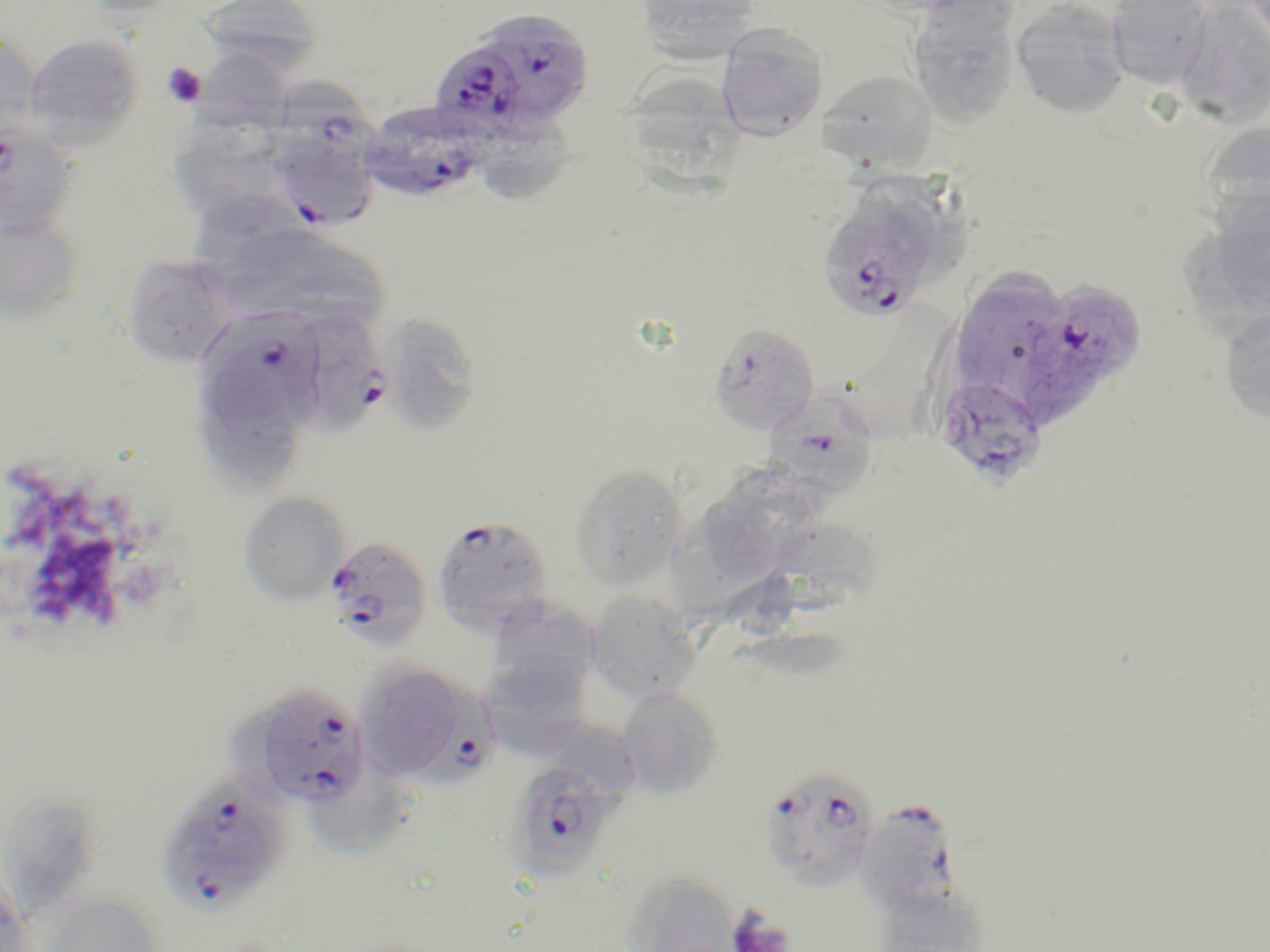

{
  "slide_level_diagnosis": "Plasmodium falciparum",
  "uninfected_red_blood_cell_locations": "approximate bounding boxes as named x1/y1/x2/y2 corners in pixels: (x1=72, y1=0, x2=190, y2=20), (x1=200, y1=0, x2=321, y2=78), (x1=634, y1=0, x2=763, y2=63), (x1=851, y1=0, x2=981, y2=15), (x1=1009, y1=1, x2=1131, y2=119), (x1=1106, y1=1, x2=1214, y2=91), (x1=1177, y1=1, x2=1270, y2=124), (x1=906, y1=4, x2=1022, y2=129), (x1=716, y1=24, x2=828, y2=141), (x1=0, y1=32, x2=43, y2=138), (x1=24, y1=34, x2=143, y2=150), (x1=194, y1=49, x2=292, y2=135), (x1=627, y1=69, x2=753, y2=204), (x1=817, y1=70, x2=937, y2=171), (x1=482, y1=106, x2=581, y2=204), (x1=176, y1=118, x2=279, y2=234), (x1=1202, y1=118, x2=1269, y2=238), (x1=199, y1=198, x2=313, y2=299), (x1=0, y1=213, x2=85, y2=326), (x1=278, y1=242, x2=390, y2=337), (x1=121, y1=254, x2=240, y2=368), (x1=954, y1=266, x2=1066, y2=381), (x1=1218, y1=306, x2=1270, y2=423), (x1=379, y1=312, x2=485, y2=438), (x1=199, y1=397, x2=302, y2=484), (x1=569, y1=463, x2=689, y2=592), (x1=729, y1=463, x2=842, y2=523), (x1=239, y1=491, x2=351, y2=606), (x1=705, y1=492, x2=789, y2=586), (x1=774, y1=517, x2=890, y2=596), (x1=668, y1=518, x2=766, y2=623), (x1=585, y1=590, x2=703, y2=705), (x1=484, y1=600, x2=599, y2=702), (x1=485, y1=656, x2=586, y2=757), (x1=352, y1=660, x2=463, y2=784), (x1=614, y1=687, x2=725, y2=799), (x1=544, y1=716, x2=637, y2=811), (x1=311, y1=757, x2=408, y2=855), (x1=12, y1=791, x2=105, y2=917), (x1=621, y1=871, x2=740, y2=952), (x1=0, y1=880, x2=33, y2=952), (x1=42, y1=892, x2=167, y2=951), (x1=871, y1=897, x2=987, y2=952)",
  "modality": "light microscopy",
  "field_of_view": "single",
  "plasmodium_falciparum_infected_red_blood_cell_locations": "approximate bounding boxes as named x1/y1/x2/y2 corners in pixels: (x1=483, y1=11, x2=597, y2=129), (x1=438, y1=45, x2=529, y2=156), (x1=271, y1=73, x2=378, y2=162), (x1=360, y1=100, x2=489, y2=203), (x1=265, y1=119, x2=381, y2=233), (x1=0, y1=120, x2=81, y2=238), (x1=816, y1=194, x2=943, y2=322), (x1=1015, y1=274, x2=1149, y2=425), (x1=202, y1=309, x2=327, y2=423), (x1=292, y1=309, x2=387, y2=438), (x1=708, y1=323, x2=819, y2=435), (x1=933, y1=374, x2=1049, y2=490), (x1=775, y1=400, x2=878, y2=496), (x1=432, y1=514, x2=555, y2=632), (x1=323, y1=536, x2=433, y2=654), (x1=233, y1=682, x2=370, y2=809), (x1=413, y1=683, x2=502, y2=798), (x1=504, y1=760, x2=624, y2=883), (x1=759, y1=764, x2=880, y2=891), (x1=154, y1=774, x2=291, y2=916), (x1=855, y1=798, x2=963, y2=916)",
  "image_size": "1270×952 pixels",
  "platelet_locations": "approximate bounding boxes as named x1/y1/x2/y2 corners in pixels: (x1=162, y1=63, x2=206, y2=107), (x1=727, y1=908, x2=796, y2=952)",
  "stain": "May-Grünwald-Giemsa",
  "magnification": "1000x",
  "preparation": "thin blood smear"
}